Name the parasite shown.
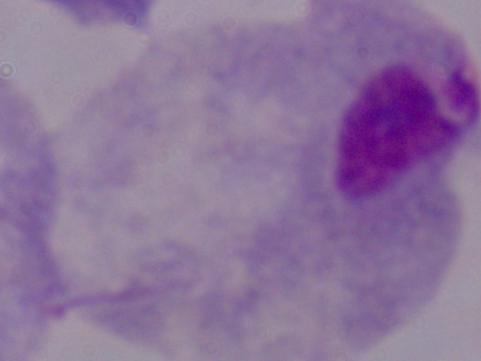
This is a trichomonad.

Photomicrograph. Captured at 1000x magnification.